Classify this cell by malaria status.
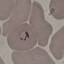

It is parasitized.

Summary:
  - Capture: smartphone through the microscope eyepiece
  - Preparation: thin smear
  - Image type: automatically extracted cell patch, resized to 64 × 64 pixels
  - Stain: Giemsa